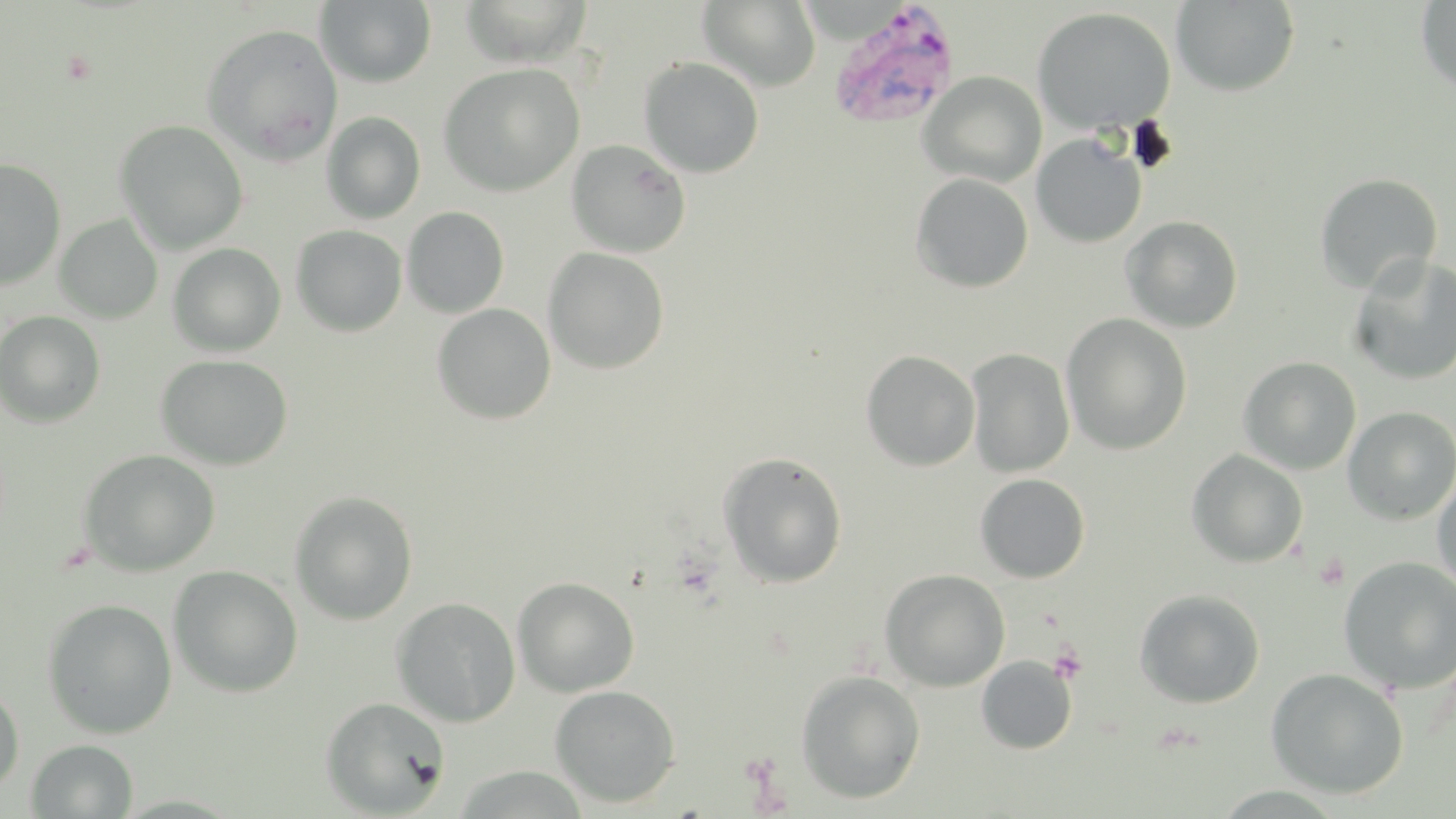
Summary:
  - Coordinate format: approximate bounding boxes as [x1, y1, x2, y2] in pixels
  - Platelet locations: [1313, 552, 1349, 590], [1049, 644, 1089, 684]
  - Plasmodium vivax-infected red blood cell locations: [827, 2, 960, 129]
  - Uninfected red blood cell locations: [697, 0, 821, 91], [315, 1, 437, 88], [457, 1, 596, 68], [1170, 1, 1300, 97], [1415, 1, 1456, 95], [1031, 7, 1176, 134], [201, 24, 343, 164], [639, 58, 764, 178], [438, 63, 585, 197], [919, 72, 1046, 188], [321, 112, 426, 224], [114, 120, 249, 254], [1031, 133, 1147, 248], [566, 139, 691, 258], [0, 158, 67, 290], [910, 172, 1034, 293], [1314, 173, 1443, 295], [401, 206, 509, 319], [55, 215, 163, 324], [1120, 215, 1244, 333], [291, 225, 407, 337], [167, 243, 286, 357], [542, 247, 670, 375], [1348, 255, 1456, 386], [431, 304, 556, 425], [0, 311, 106, 428], [1061, 313, 1193, 455], [965, 348, 1075, 477], [860, 350, 981, 471], [155, 354, 293, 470], [1238, 356, 1362, 475], [1342, 406, 1456, 525], [78, 449, 220, 576], [1186, 449, 1309, 568], [718, 451, 848, 588], [1431, 472, 1456, 598], [974, 473, 1091, 583], [289, 491, 418, 625], [1337, 556, 1456, 694], [168, 565, 303, 698], [879, 568, 1011, 691], [512, 576, 640, 697], [1134, 589, 1266, 708], [391, 597, 520, 727], [41, 598, 178, 739], [976, 655, 1077, 754], [1266, 667, 1409, 799], [795, 670, 926, 804], [0, 680, 25, 795], [549, 685, 681, 808], [319, 696, 450, 817], [26, 739, 138, 818]
  - Slide-level diagnosis: Plasmodium vivax
  - Preparation: thin blood smear
  - Image size: 1456×819 pixels
  - Modality: optical microscopy
  - Stain: May-Grünwald-Giemsa
  - Magnification: 1000x
  - Field of view: single